Describe the morphology of the erythrocytes.
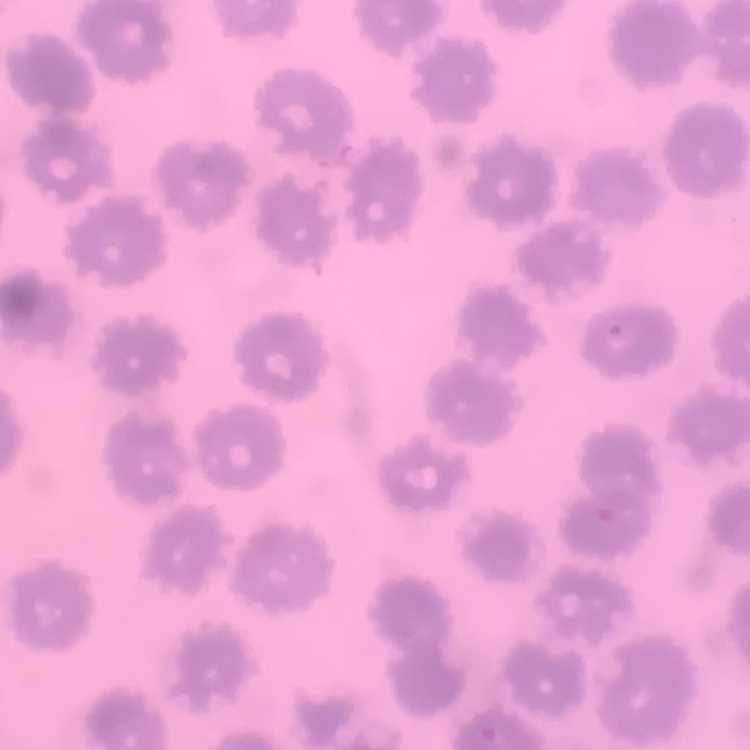
No rouleaux formation.

image type = one tile cut from a larger photomicrograph
stain = Field's or Giemsa
preparation = thin blood film